Locate every blood parasite and identify its species.
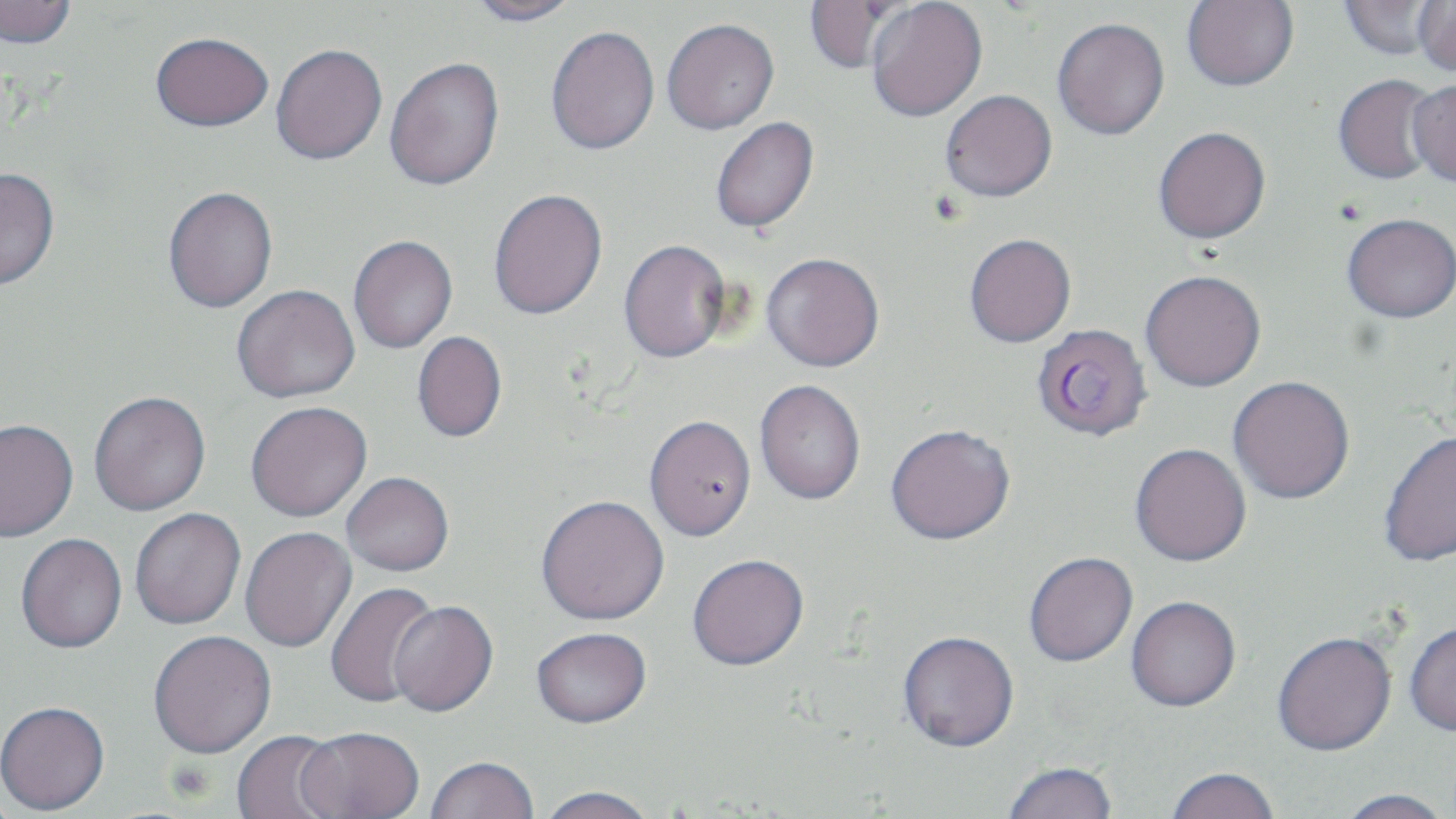

Approximate bounding boxes as [x1, y1, x2, y2] in pixels.
Plasmodium falciparum-infected red blood cells: [1031, 323, 1153, 442].
No Plasmodium ovale, Plasmodium malariae, Plasmodium vivax, Babesia divergens, or Trypanosoma brucei observed.

slide-level diagnosis = Plasmodium falciparum
preparation = thin blood smear
field of view = one of a larger specimen
stain = May-Grünwald-Giemsa
image size = 1456×819 pixels
magnification = 1000x
uninfected red blood cell locations = approximate bounding boxes as [x1, y1, x2, y2] in pixels: [0, 0, 78, 50], [466, 0, 582, 26], [804, 0, 910, 74], [866, 0, 987, 122], [1182, 0, 1299, 91], [1337, 1, 1446, 60], [1380, 1, 1456, 79], [1412, 1, 1456, 77], [1052, 17, 1170, 140], [662, 18, 779, 134], [545, 25, 660, 155], [150, 32, 273, 131], [271, 43, 388, 165], [384, 56, 505, 191], [1332, 73, 1442, 185], [1408, 78, 1456, 186], [940, 89, 1057, 202], [710, 116, 819, 233], [1153, 126, 1271, 244], [0, 167, 60, 290], [163, 186, 278, 313], [489, 188, 608, 320], [1342, 212, 1456, 324], [964, 232, 1076, 347], [348, 234, 458, 353], [619, 238, 732, 363], [761, 252, 884, 372], [1140, 270, 1267, 392], [231, 284, 361, 403], [411, 331, 506, 443], [1228, 377, 1355, 505], [754, 379, 866, 506], [88, 391, 211, 516], [246, 401, 372, 522], [644, 415, 756, 542], [0, 418, 79, 542], [885, 424, 1017, 546], [1379, 429, 1456, 568], [1130, 444, 1252, 568], [342, 473, 454, 576], [536, 496, 670, 626], [130, 508, 246, 630], [240, 527, 357, 652], [15, 533, 127, 655], [1024, 553, 1139, 669], [687, 555, 809, 673], [326, 581, 442, 709], [1126, 597, 1242, 714], [388, 602, 498, 718], [1404, 620, 1456, 737], [531, 629, 652, 732], [148, 631, 277, 759], [898, 633, 1019, 754], [1273, 633, 1397, 758], [0, 702, 110, 816], [296, 728, 424, 818], [231, 730, 345, 819], [425, 758, 539, 818], [1001, 762, 1118, 819], [1165, 768, 1281, 819], [533, 788, 660, 819], [1333, 789, 1454, 819]
modality = optical microscopy